Outline each uninfected red blood cell.
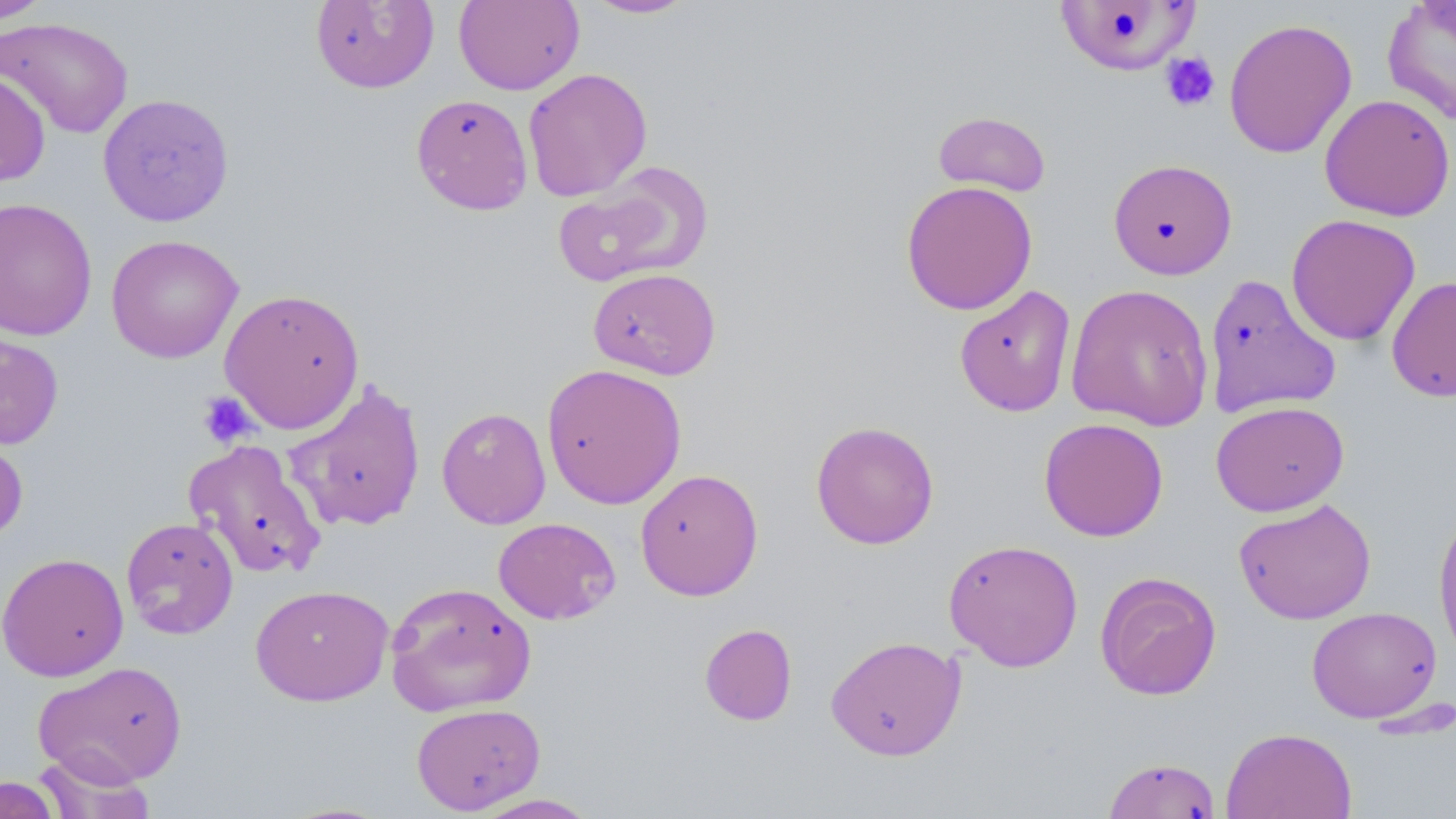

Approximate bounding boxes as (x1,y1)-(x2,y2) corner pairs in pixels.
Uninfected red blood cells: (1,0)-(55,24), (584,0)-(697,19), (310,1)-(439,93), (453,1)-(584,95), (1054,1)-(1201,76), (1381,1)-(1456,125), (0,16)-(134,139), (1223,16)-(1357,159), (522,68)-(653,201), (0,69)-(51,186), (97,93)-(235,226), (411,93)-(533,215), (1319,93)-(1455,221), (933,110)-(1051,197), (1108,158)-(1237,279), (552,163)-(710,288), (900,180)-(1038,316), (0,196)-(97,341), (1286,214)-(1421,346), (106,234)-(243,363), (588,267)-(721,380), (1203,272)-(1342,420), (1387,275)-(1456,402), (1065,283)-(1215,432), (953,284)-(1077,417), (219,288)-(366,433), (0,329)-(64,450), (541,363)-(687,509), (285,379)-(427,533), (1211,400)-(1349,517), (437,407)-(552,529), (1039,417)-(1168,542), (811,420)-(939,549), (0,429)-(29,545), (183,439)-(326,580), (635,468)-(764,601), (1233,499)-(1376,625), (1433,509)-(1456,664), (120,517)-(238,639), (493,517)-(621,625), (943,538)-(1084,672), (0,552)-(128,682), (1095,571)-(1222,700), (384,581)-(538,717), (250,584)-(394,706), (1306,606)-(1442,723), (699,623)-(798,726), (825,635)-(966,761), (32,660)-(190,786), (411,703)-(546,815), (1221,727)-(1358,819), (34,746)-(156,818), (1103,756)-(1221,819), (0,775)-(63,819), (467,793)-(601,818), (276,801)-(397,818).

Platelet locations: (1160,51)-(1220,112), (197,391)-(257,448). Slide-level diagnosis: no evidence of blood parasites. May-Grünwald-Giemsa-stained preparation. Image is 1456×819 pixels. Thin blood smear. Light microscopy. Captured at 1000x magnification. One field of a larger specimen.